Classify this cell by malaria status.
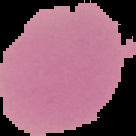
Uninfected.

From a thin blood film. The area outside the segmented cell region is set to black. Image is 136×136 pixels.